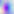

magnification = 400x
modality = photomicrograph
identification = Toxoplasma gondii